Assess this cell for malaria.
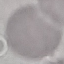

It is uninfected.

Giemsa-stained preparation. Thin blood film. Photographed with a smartphone camera at the microscope eyepiece. Automatically extracted cell patch, resized to 64 × 64 pixels.